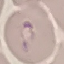
malaria status = parasitized
stain = Giemsa
preparation = thin blood film
image type = automatically extracted cell patch, resized to 64 × 64 pixels
capture = smartphone camera at the microscope eyepiece